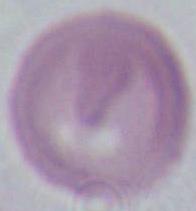

Summary:
  - Modality: micrograph
  - Magnification: 1000x
  - Identification: erythrocyte